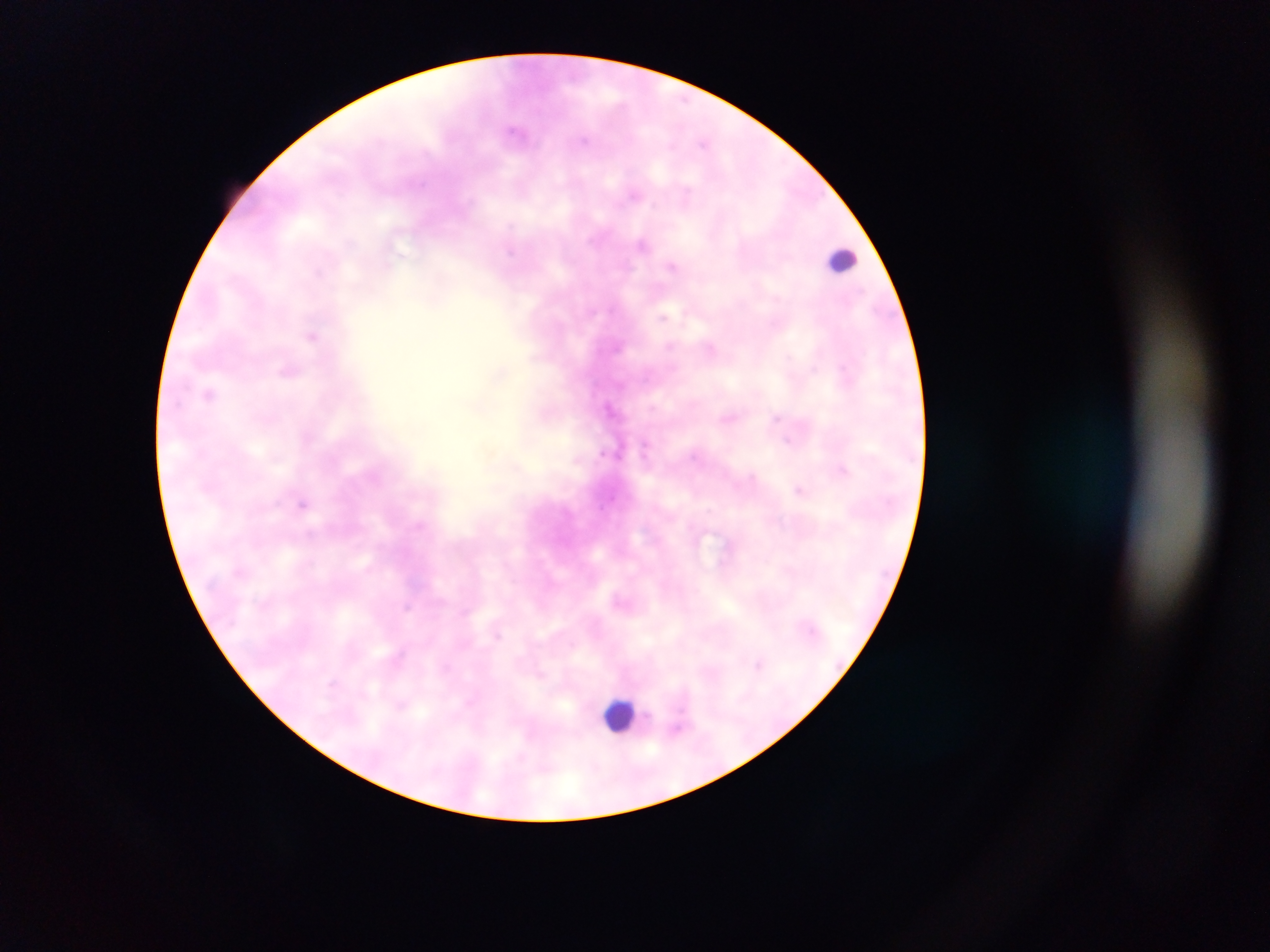

Approximate centers as x y in pixels.
Summary:
  - Malaria parasite locations: 585 140; 704 143; 635 196; 642 243; 672 267; 317 272; 664 317; 312 336; 669 345; 711 349; 287 369; 208 394; 610 408; 777 416; 788 440; 842 469; 800 490; 303 503; 309 534; 408 607; 497 636; 759 663; 331 684; 401 706
  - Leukocyte locations: 843 261; 620 715
  - Preparation: thick blood film
  - Country: Ghana
  - Image size: 1270×952 pixels
  - Field of view: single
  - Capture: mobile-phone photograph through a microscope